Locate and identify every blood parasite.
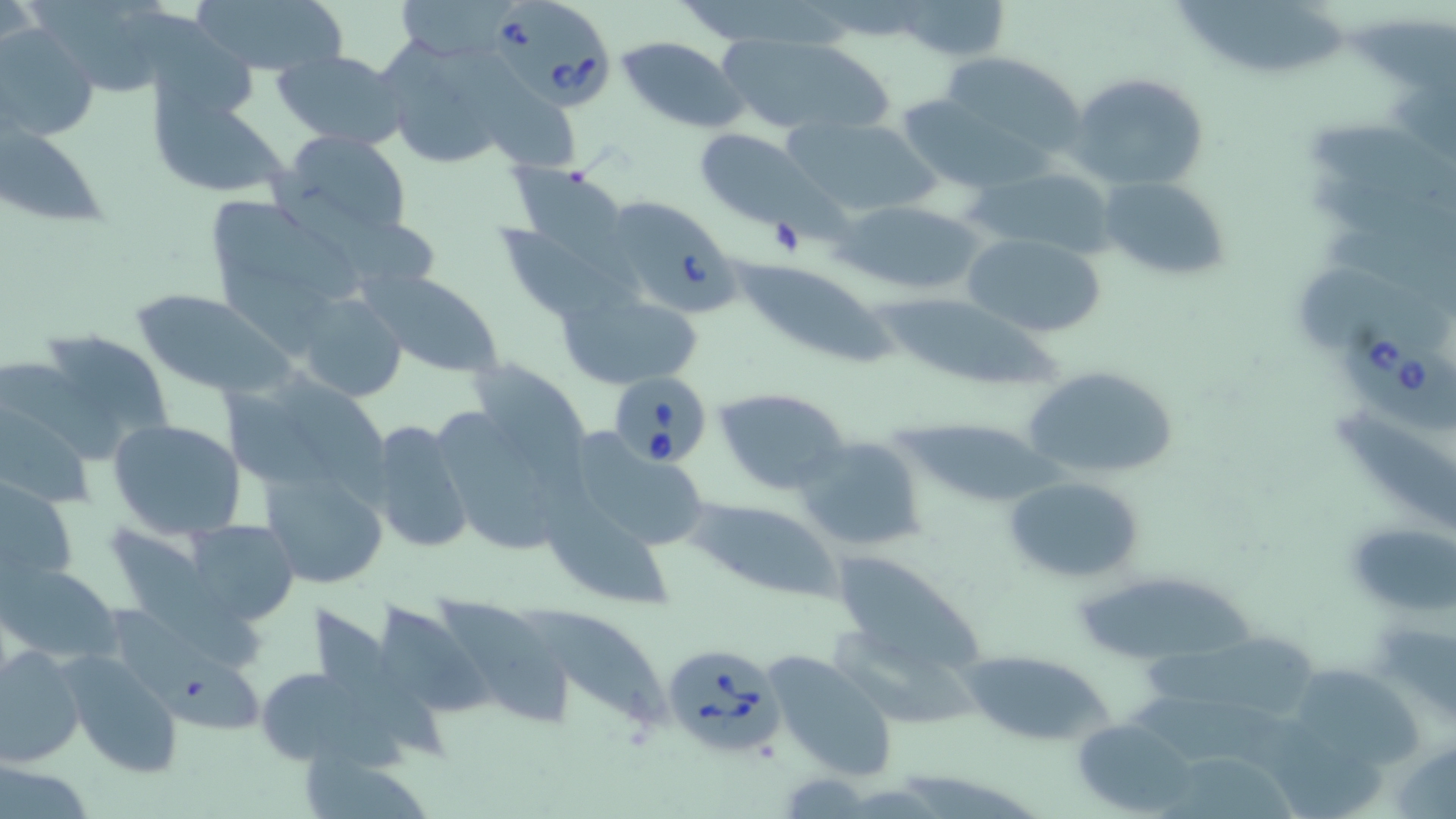

Approximate bounding boxes as named x1/y1/x2/y2 corners in pixels.
Babesia divergens-infected red blood cells: (x1=491, y1=0, x2=612, y2=114), (x1=597, y1=195, x2=745, y2=321), (x1=1342, y1=318, x2=1455, y2=436), (x1=609, y1=373, x2=715, y2=471), (x1=664, y1=647, x2=785, y2=755).
No Plasmodium falciparum, Plasmodium ovale, Plasmodium malariae, Plasmodium vivax, or Trypanosoma brucei observed.

Uninfected red blood cell locations: (x1=193, y1=0, x2=349, y2=78), (x1=1178, y1=0, x2=1351, y2=76), (x1=895, y1=1, x2=1010, y2=61), (x1=130, y1=9, x2=260, y2=113), (x1=1350, y1=17, x2=1456, y2=83), (x1=1, y1=21, x2=99, y2=143), (x1=712, y1=32, x2=893, y2=137), (x1=617, y1=36, x2=747, y2=132), (x1=369, y1=41, x2=517, y2=165), (x1=273, y1=49, x2=409, y2=150), (x1=936, y1=52, x2=1089, y2=163), (x1=1071, y1=69, x2=1212, y2=191), (x1=483, y1=85, x2=578, y2=172), (x1=157, y1=93, x2=291, y2=199), (x1=3, y1=118, x2=114, y2=222), (x1=787, y1=118, x2=940, y2=217), (x1=1312, y1=122, x2=1456, y2=218), (x1=694, y1=129, x2=830, y2=233), (x1=274, y1=131, x2=415, y2=241), (x1=507, y1=165, x2=629, y2=260), (x1=969, y1=165, x2=1118, y2=260), (x1=1098, y1=175, x2=1233, y2=281), (x1=209, y1=197, x2=358, y2=294), (x1=834, y1=199, x2=987, y2=297), (x1=489, y1=220, x2=629, y2=322), (x1=965, y1=233, x2=1106, y2=337), (x1=730, y1=261, x2=892, y2=367), (x1=1292, y1=265, x2=1456, y2=347), (x1=360, y1=269, x2=506, y2=380), (x1=557, y1=286, x2=706, y2=389), (x1=867, y1=288, x2=1072, y2=393), (x1=131, y1=289, x2=292, y2=399), (x1=292, y1=292, x2=410, y2=404), (x1=31, y1=328, x2=176, y2=463), (x1=1021, y1=363, x2=1180, y2=482), (x1=222, y1=373, x2=396, y2=504), (x1=715, y1=387, x2=852, y2=493), (x1=0, y1=392, x2=96, y2=511), (x1=423, y1=396, x2=592, y2=558), (x1=1331, y1=405, x2=1456, y2=530), (x1=895, y1=416, x2=1053, y2=508), (x1=107, y1=417, x2=246, y2=539), (x1=367, y1=418, x2=473, y2=556), (x1=554, y1=429, x2=715, y2=559), (x1=794, y1=434, x2=926, y2=556), (x1=258, y1=466, x2=389, y2=591), (x1=0, y1=474, x2=79, y2=595), (x1=1004, y1=475, x2=1145, y2=584), (x1=537, y1=494, x2=686, y2=611), (x1=688, y1=498, x2=842, y2=600), (x1=185, y1=519, x2=298, y2=626), (x1=1347, y1=521, x2=1455, y2=616), (x1=114, y1=527, x2=264, y2=666), (x1=835, y1=551, x2=988, y2=669), (x1=0, y1=563, x2=121, y2=666), (x1=1078, y1=574, x2=1260, y2=660), (x1=430, y1=594, x2=573, y2=728), (x1=382, y1=602, x2=500, y2=717), (x1=530, y1=604, x2=676, y2=731), (x1=311, y1=606, x2=449, y2=763), (x1=1144, y1=630, x2=1323, y2=731), (x1=0, y1=648, x2=85, y2=770), (x1=763, y1=650, x2=901, y2=784), (x1=62, y1=651, x2=186, y2=778), (x1=957, y1=651, x2=1115, y2=747), (x1=162, y1=659, x2=268, y2=735), (x1=255, y1=663, x2=366, y2=769), (x1=1290, y1=663, x2=1432, y2=764), (x1=1073, y1=718, x2=1198, y2=815), (x1=1170, y1=756, x2=1299, y2=819), (x1=0, y1=759, x2=94, y2=817). Slide-level diagnosis: Babesia divergens. Light microscopy. Thin blood smear. May-Grünwald-Giemsa stain. Image is 1456×819 pixels. One field of a larger specimen. 1000x magnification.